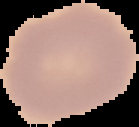

Summary:
  - Image size: 139×127 pixels
  - Preparation: thin blood smear
  - Image type: segmented cell region with the area outside set to black
  - Result: no Plasmodium parasites seen